Assess this cell for malaria.
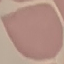

It is uninfected.

Acquired by smartphone through the microscope eyepiece. Thin blood smear. Giemsa stain. Automatically extracted cell patch, resized to 64 × 64 pixels.